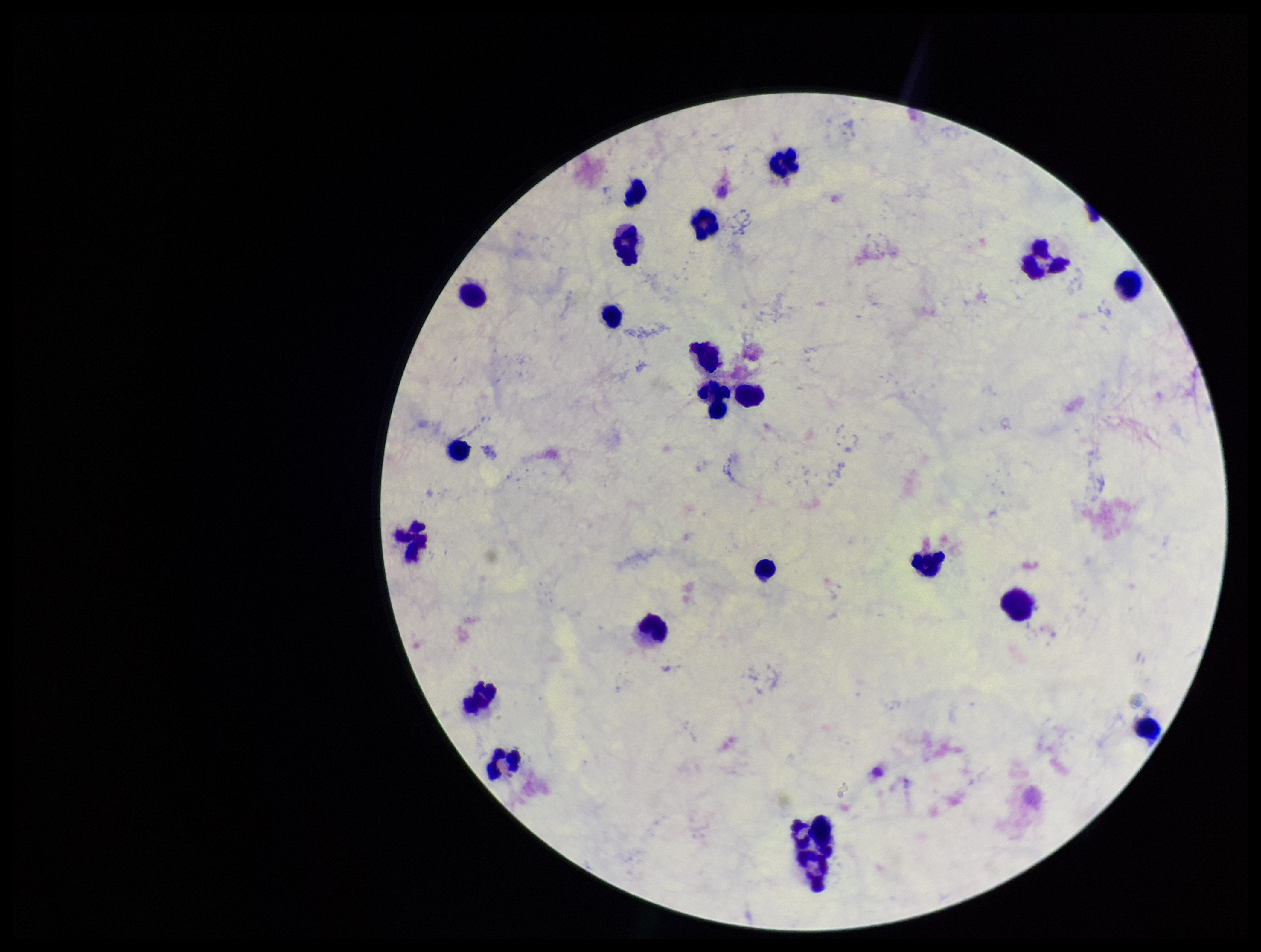
{
  "parasite_count": 0,
  "patient_malaria_status": "negative",
  "capture": "smartphone photograph through the microscope eyepiece",
  "leukocyte_count": 22,
  "plasmodium_parasites": "none detected",
  "image_size": "1261×952 pixels",
  "field_of_view": "one from this slide",
  "preparation": "thick blood smear",
  "stain": "Giemsa"
}